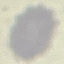

Result: negative for malaria parasites. Cell patch, automatically extracted from a larger field of view and resized to 64 × 64 pixels. Thin smear of blood. Giemsa-stained preparation. Acquired by smartphone through the microscope eyepiece.